Give the position of every Plasmodium parasite.
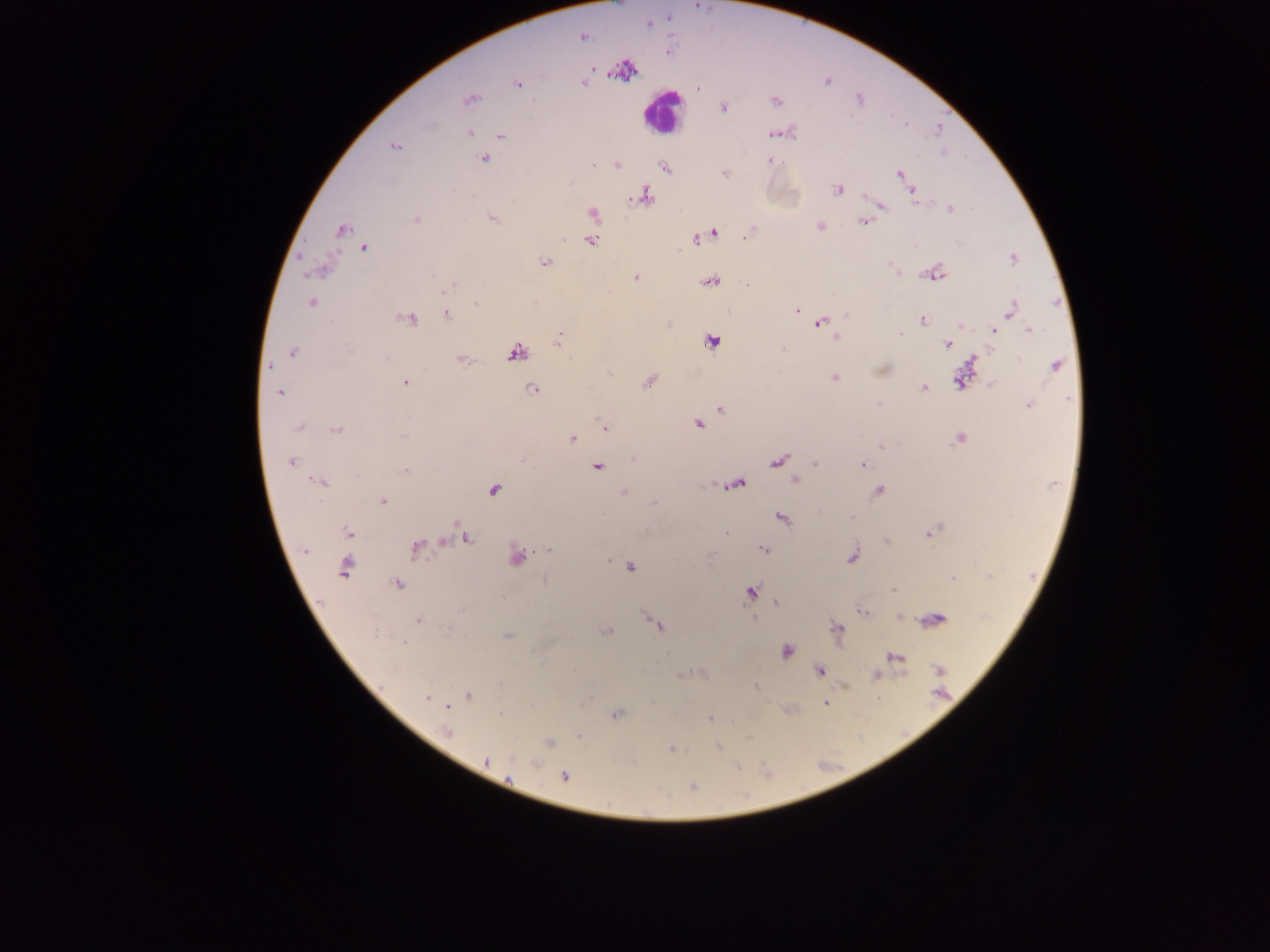
Approximate centers as (x, y) in pixels.
Plasmodium parasites: (695, 8), (648, 25), (583, 37), (594, 68), (698, 90), (723, 107), (908, 124), (470, 132), (775, 133), (500, 136), (394, 146), (484, 158), (769, 160), (594, 164), (899, 173), (836, 189), (643, 196), (915, 201), (884, 207), (593, 213), (416, 219), (863, 221), (340, 230), (748, 233), (592, 240), (696, 240), (363, 248), (1011, 258), (545, 263), (636, 277), (445, 289), (309, 304), (475, 304), (797, 310), (1011, 310), (447, 315), (924, 321), (819, 324), (993, 328), (1028, 330), (900, 335), (558, 342), (946, 344), (292, 353), (1054, 365), (268, 366), (406, 382), (648, 384), (924, 387), (532, 389), (279, 393), (1027, 405), (719, 408), (698, 423), (298, 427), (606, 428), (337, 432), (404, 436), (573, 439), (631, 458), (291, 462), (862, 465), (405, 471), (320, 483), (878, 489), (383, 501), (853, 518), (940, 526), (349, 532), (927, 534), (467, 539), (445, 541), (886, 541), (551, 548), (763, 549), (417, 550), (517, 557), (630, 566), (344, 567), (955, 578), (397, 584), (892, 590), (417, 619), (607, 630), (374, 635), (405, 644), (876, 676), (468, 695), (425, 696), (447, 707), (710, 718), (447, 733), (672, 750), (485, 762), (564, 775), (508, 778).

Leukocyte locations: (656, 107). Thick blood smear. Image is 1270×952 pixels. Mobile-phone photograph taken through the microscope. Single field of view. Collected in Ghana.